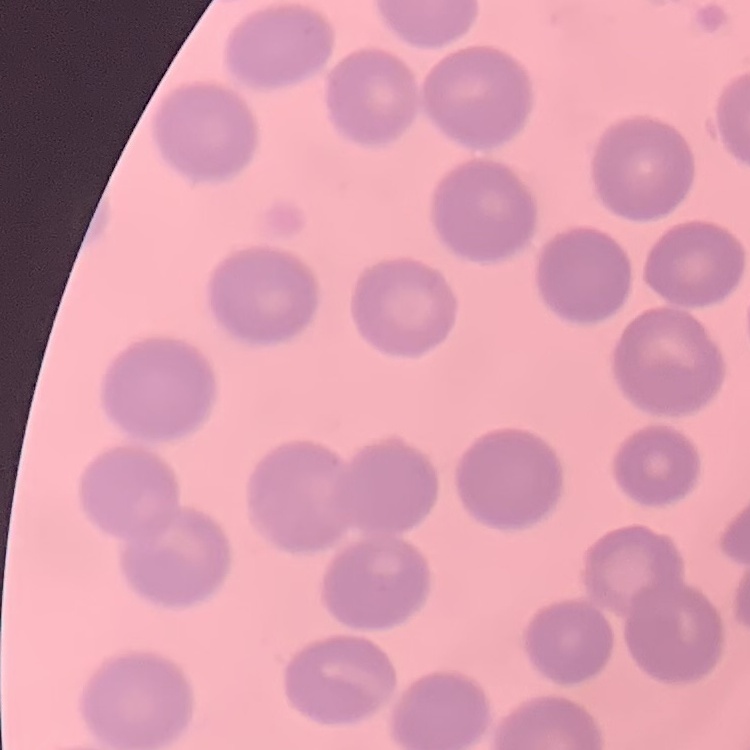
{
  "red_blood_cell_morphology": "no rouleaux formation",
  "image_type": "square crop of a larger photomicrograph",
  "stain": "Field's or Giemsa",
  "preparation": "thin blood smear"
}